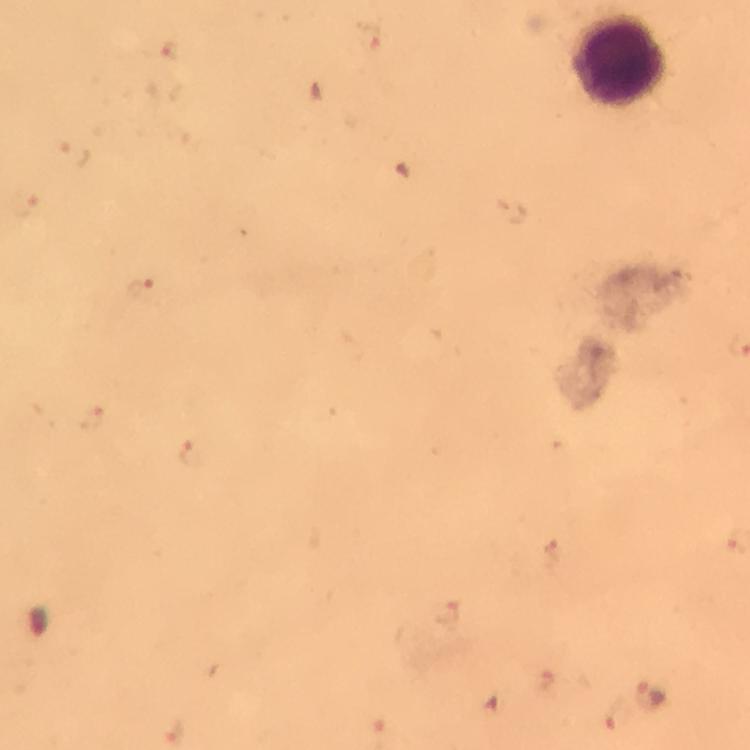
Approximate centers as [x, y] in pixels. Leukocyte locations: [619, 61]. Malaria parasite locations: [369, 37], [171, 52], [72, 155], [26, 205], [141, 289], [91, 419], [192, 454], [552, 556], [450, 614], [542, 679], [651, 694], [619, 717], [172, 732]. Image is 750×750 pixels. From a diagnostic examination for malaria. Immersion oil was used. Giemsa-stained preparation. At 100x magnification. Photographed through the microscope with a smartphone camera. Cropped region of a single field of view. Thick smear.